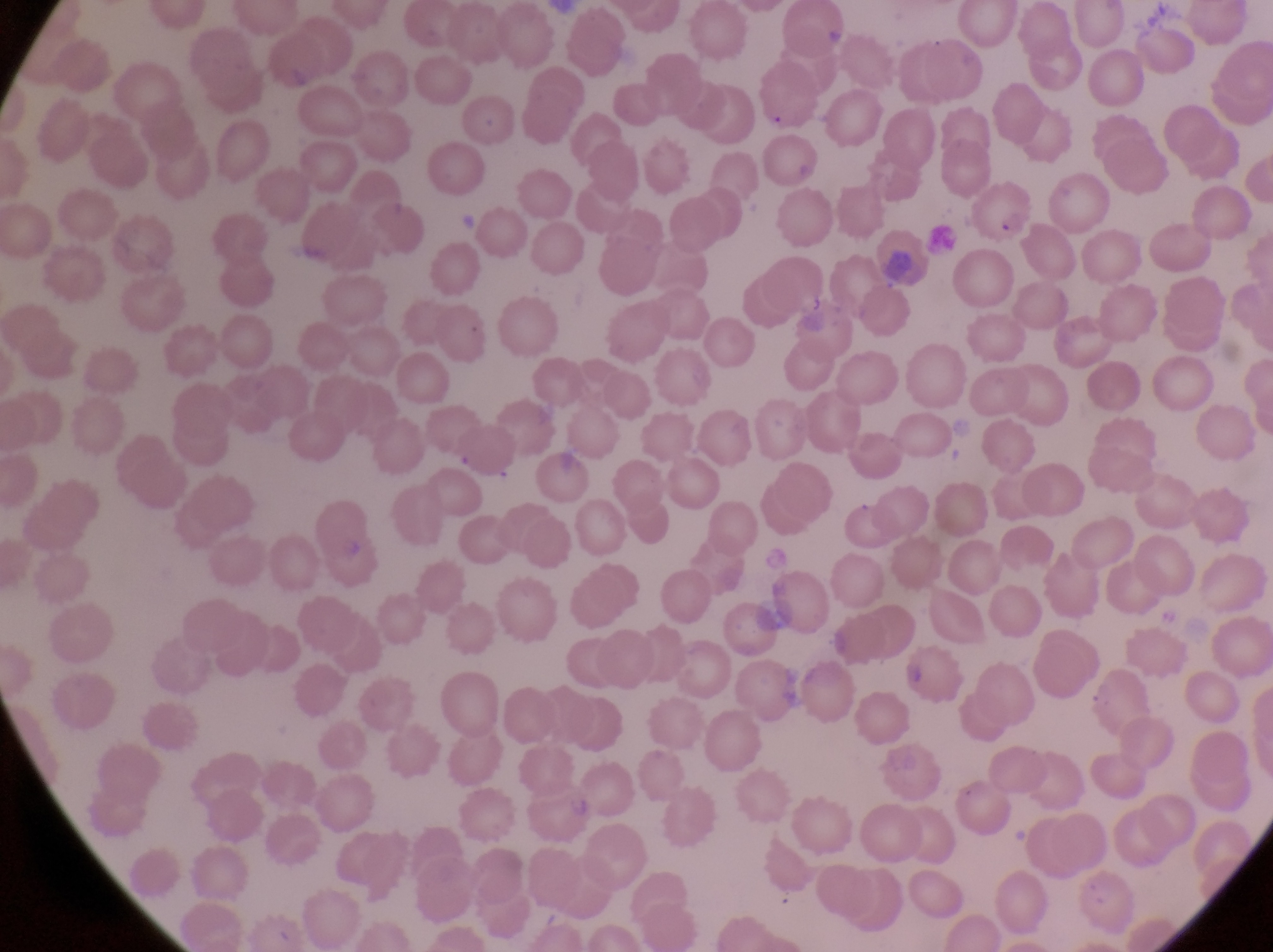
Approximate bounding boxes as (left, top, right, bottom) in pixels. Parasitised red blood cell locations: (968, 183, 1033, 241). Image is 1273×952 pixels. One field of view. Magnification of 1000x. Collected in Uganda. Thin blood film. Photographed through the eyepiece of an Olympus CX-23 microscope with a smartphone camera.